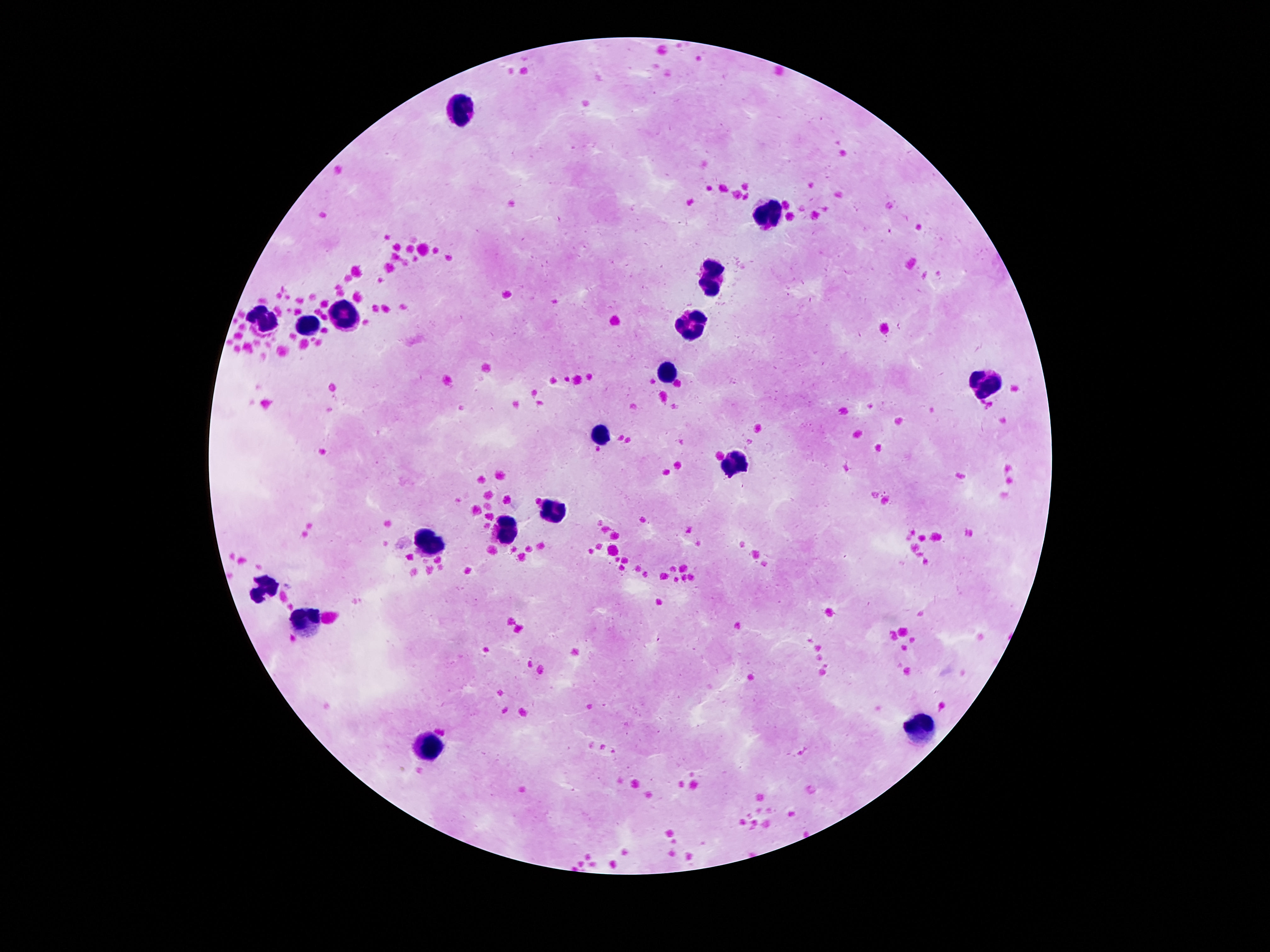
stain: Giemsa
magnification: 100x
image_size: 1270×952 pixels
leukocyte_locations: 'approximate centers as {x, y} in pixels: {462, 109}, {766, 214}, {716, 275}, {346, 313}, {267, 323}, {307, 324}, {693, 324}, {667, 369}, {983, 385}, {603, 436}, {729, 461}, {553, 509}, {507, 529}, {425, 541}, {268, 587}, {309, 619}, {921, 726}, {427, 745}'
capture: smartphone camera through the microscope eyepiece
field_of_view: single
patient_malaria_status: negative
preparation: thick blood film